Assess this cell for malaria.
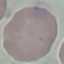
It is uninfected.

Summary:
  - Stain: Giemsa
  - Image type: automatically extracted cell patch, resized to 64 × 64 pixels
  - Preparation: thin blood film
  - Capture: smartphone through the microscope eyepiece